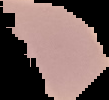

malaria status = uninfected
image size = 109×100 pixels
preparation = thin blood film
image type = cell region segmented out of the field of view; surrounding area masked to black